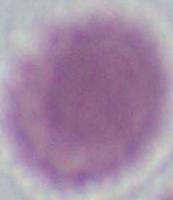
A red blood cell is seen. 1000x magnification. Photomicrograph.